Give the position of every P. falciparum parasite, noting its life-cycle stage.
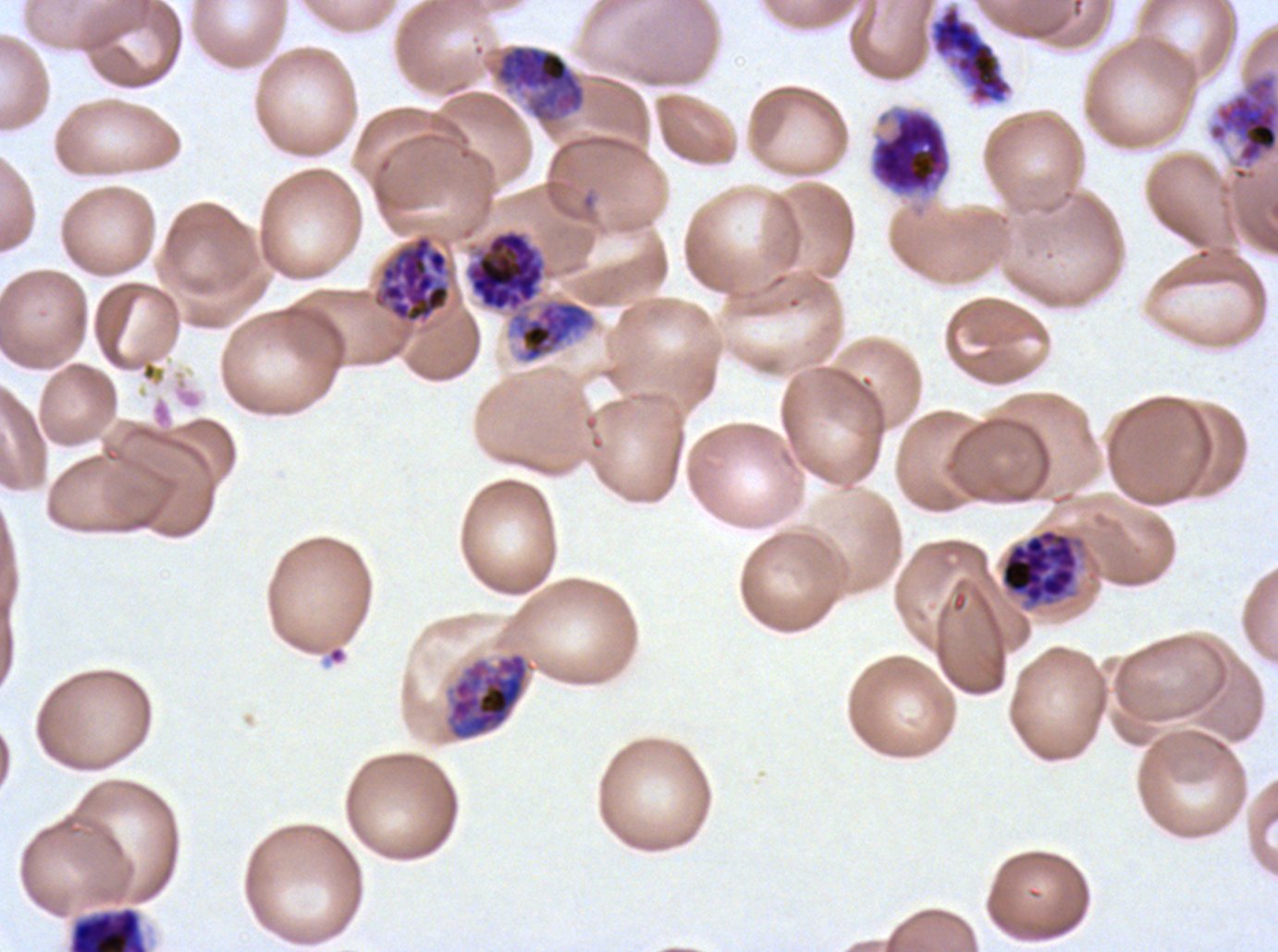
Approximate bounding boxes as (x1, y1, x2, y2) in pixels.
Early schizonts: (486, 43, 587, 126), (868, 104, 952, 201), (465, 229, 595, 363), (68, 906, 149, 951).
Late schizonts: (1207, 72, 1277, 182), (465, 229, 595, 363) (two touching objects share this one region), (1000, 528, 1079, 607), (447, 652, 529, 740).
Segmenters: (929, 4, 1013, 105), (373, 234, 451, 324).
No rings, late-ring/early-trophozoite forms, mid trophozoites, late trophozoites, or gametocytes observed.

A sub-image separated from a larger composite. Ex-vivo P. falciparum culture from a patient in The Gambia, grown for 24 to 48 hours. Giemsa stain. Thin blood smear. Life-cycle stages observed: early schizont, late schizont, segmenter. Image is 1278×952 pixels.